Give the extent of all Plasmodium falciparum-infected red blood cells.
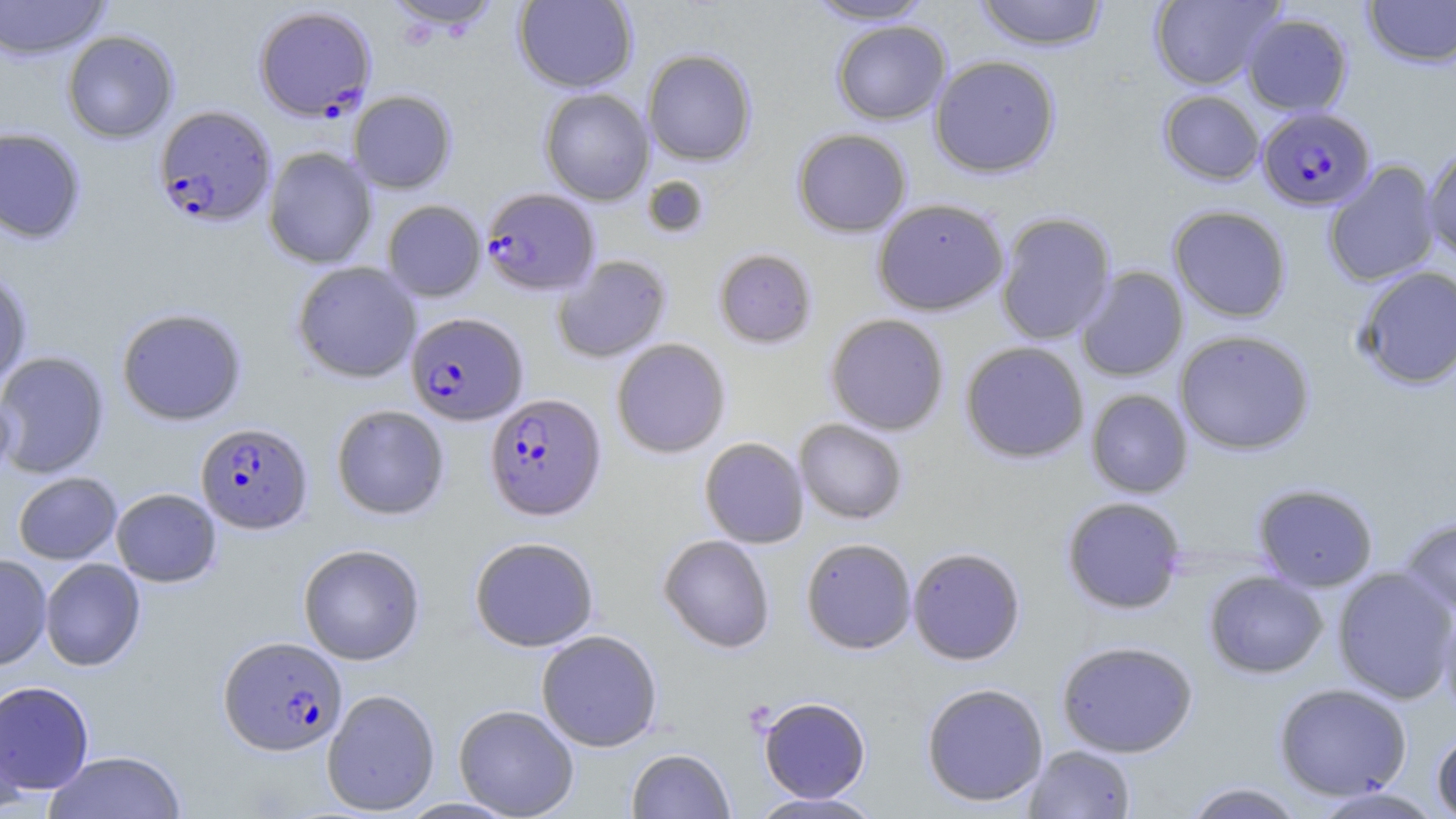
Approximate bounding boxes as [x1, y1, x2, y2] in pixels.
Plasmodium falciparum-infected red blood cells: [253, 5, 377, 122], [153, 105, 276, 228], [1257, 106, 1375, 211], [481, 188, 600, 296], [406, 312, 528, 425], [484, 393, 606, 520], [195, 422, 313, 534], [219, 636, 347, 755].

Uninfected red blood cell locations: [0, 0, 110, 61], [513, 0, 637, 93], [804, 0, 935, 24], [974, 0, 1108, 51], [1149, 0, 1283, 90], [1362, 0, 1456, 69], [384, 1, 503, 35], [1242, 12, 1353, 116], [831, 20, 951, 125], [62, 30, 179, 143], [642, 49, 756, 166], [929, 55, 1061, 178], [539, 88, 654, 205], [348, 90, 457, 194], [1158, 90, 1265, 185], [0, 126, 86, 244], [792, 128, 911, 237], [1423, 144, 1456, 261], [263, 146, 378, 269], [1322, 161, 1440, 288], [642, 175, 710, 239], [871, 198, 1010, 316], [382, 200, 486, 302], [1168, 205, 1292, 322], [995, 212, 1116, 345], [713, 248, 818, 348], [552, 255, 672, 363], [291, 261, 422, 383], [1075, 266, 1188, 382], [1353, 266, 1456, 390], [0, 270, 33, 388], [116, 307, 247, 426], [825, 313, 949, 436], [1174, 329, 1315, 455], [611, 338, 730, 458], [960, 341, 1089, 463], [0, 351, 110, 479], [0, 381, 17, 492], [1085, 389, 1193, 498], [331, 404, 450, 521], [794, 419, 908, 524], [699, 437, 809, 548], [12, 472, 122, 564], [1253, 483, 1378, 592], [111, 488, 221, 587], [1061, 496, 1186, 615], [1399, 517, 1456, 616], [658, 534, 775, 653], [469, 536, 600, 652], [800, 537, 917, 654], [297, 543, 425, 665], [907, 546, 1026, 665], [0, 554, 52, 670], [40, 558, 146, 671], [1331, 566, 1456, 703], [1204, 570, 1328, 679], [1439, 603, 1456, 722], [536, 629, 663, 751], [1056, 640, 1198, 758], [0, 681, 95, 795], [921, 682, 1049, 806], [1273, 683, 1412, 801], [322, 688, 440, 815], [757, 696, 872, 802], [0, 698, 27, 816], [453, 704, 579, 818], [1431, 728, 1456, 818], [1024, 744, 1136, 818], [626, 747, 735, 819], [43, 751, 186, 818], [1181, 782, 1308, 819], [1309, 786, 1447, 818], [747, 792, 886, 818]. Slide-level diagnosis: Plasmodium falciparum. Captured at 1000x magnification. Thin blood film. Image is 1456×819 pixels. May-Grünwald-Giemsa stain. Light microscopy. Single field of view.